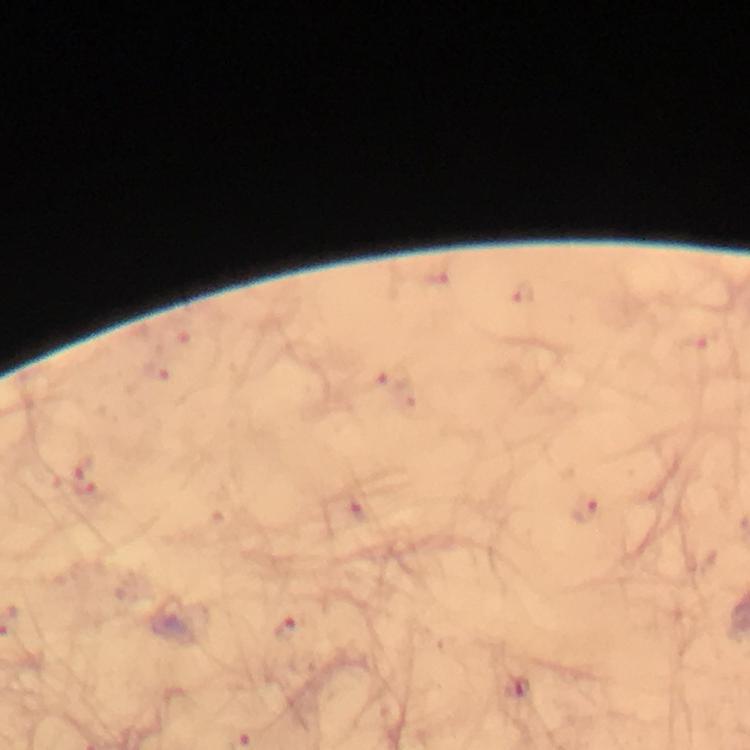 Approximate centers as (x, y) in pixels. Malaria parasite locations: (522, 290), (697, 340), (392, 377), (85, 475), (584, 508), (286, 630), (523, 688). Image is 750×750 pixels. Photographed with a smartphone mounted on the microscope. From a diagnostic examination for malaria. Giemsa-stained preparation. At 100x magnification. Thick blood film. Immersion oil applied. A crop from one field of view.